Report the malaria status of this cell.
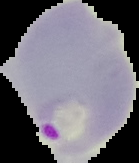

It is parasitized.

Summary:
  - Image size: 139×163 pixels
  - Image type: segmented cell region on a black background
  - Preparation: thin blood smear